Assess this cell for malaria.
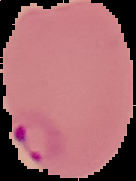

It is parasitized.

{
  "image_size": "136×181 pixels",
  "preparation": "thin blood smear",
  "image_type": "segmented cell region on a black background"
}